Classify this cell by malaria status.
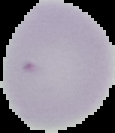
Uninfected.

Summary:
  - Preparation: thin blood smear
  - Image type: cell region segmented out of the field of view; surrounding area masked to black
  - Image size: 115×133 pixels